Assess for Plasmodium parasites.
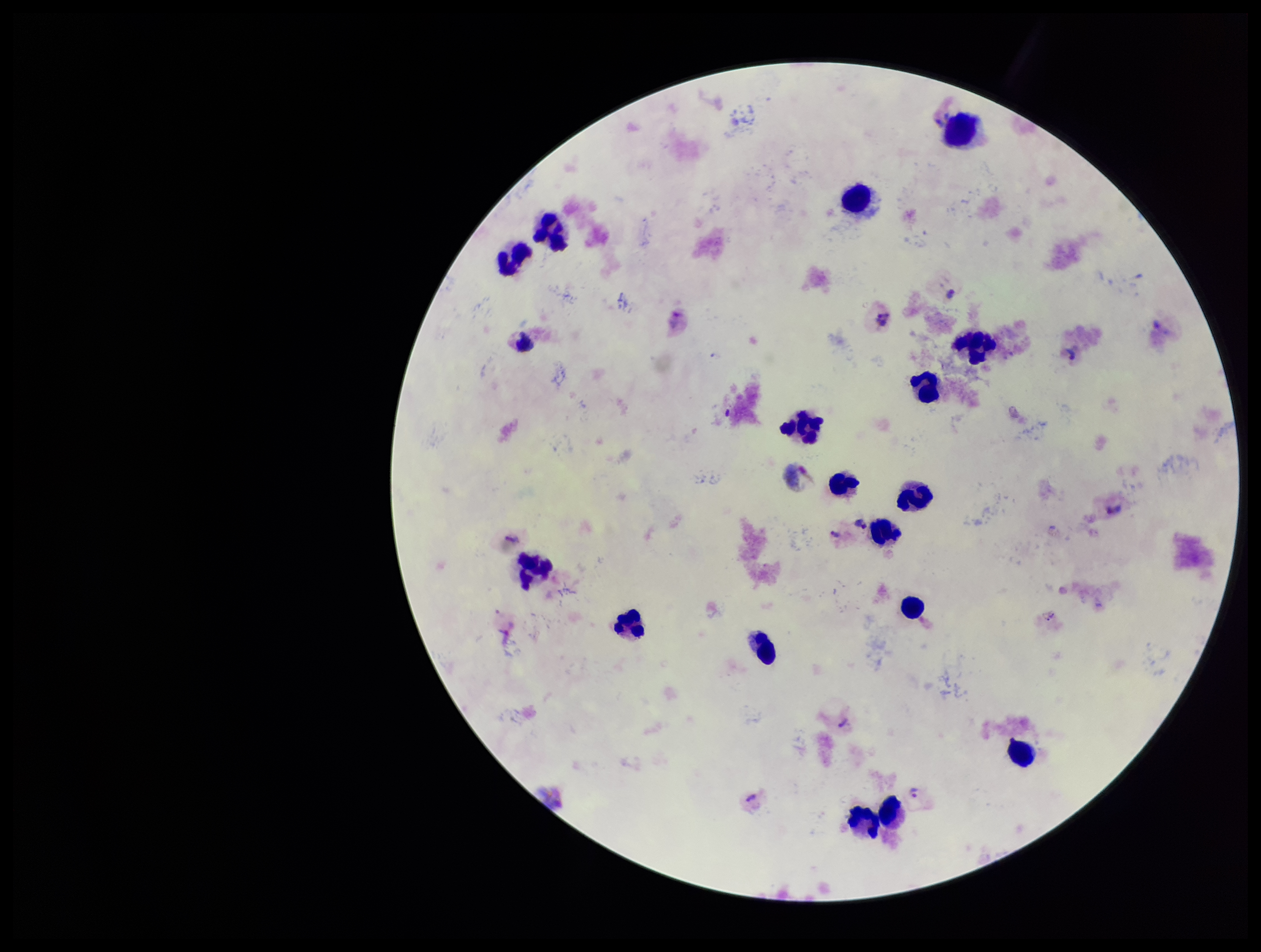

Detected.

Summary:
  - Species reported for this patient: Plasmodium vivax
  - Stain: Giemsa
  - Patient malaria status: positive
  - Leukocyte count: 17
  - Parasite count: 4
  - Image size: 1261×952 pixels
  - Field of view: one from this slide
  - Capture: smartphone photograph through the microscope eyepiece
  - Preparation: thick